Report the malaria status.
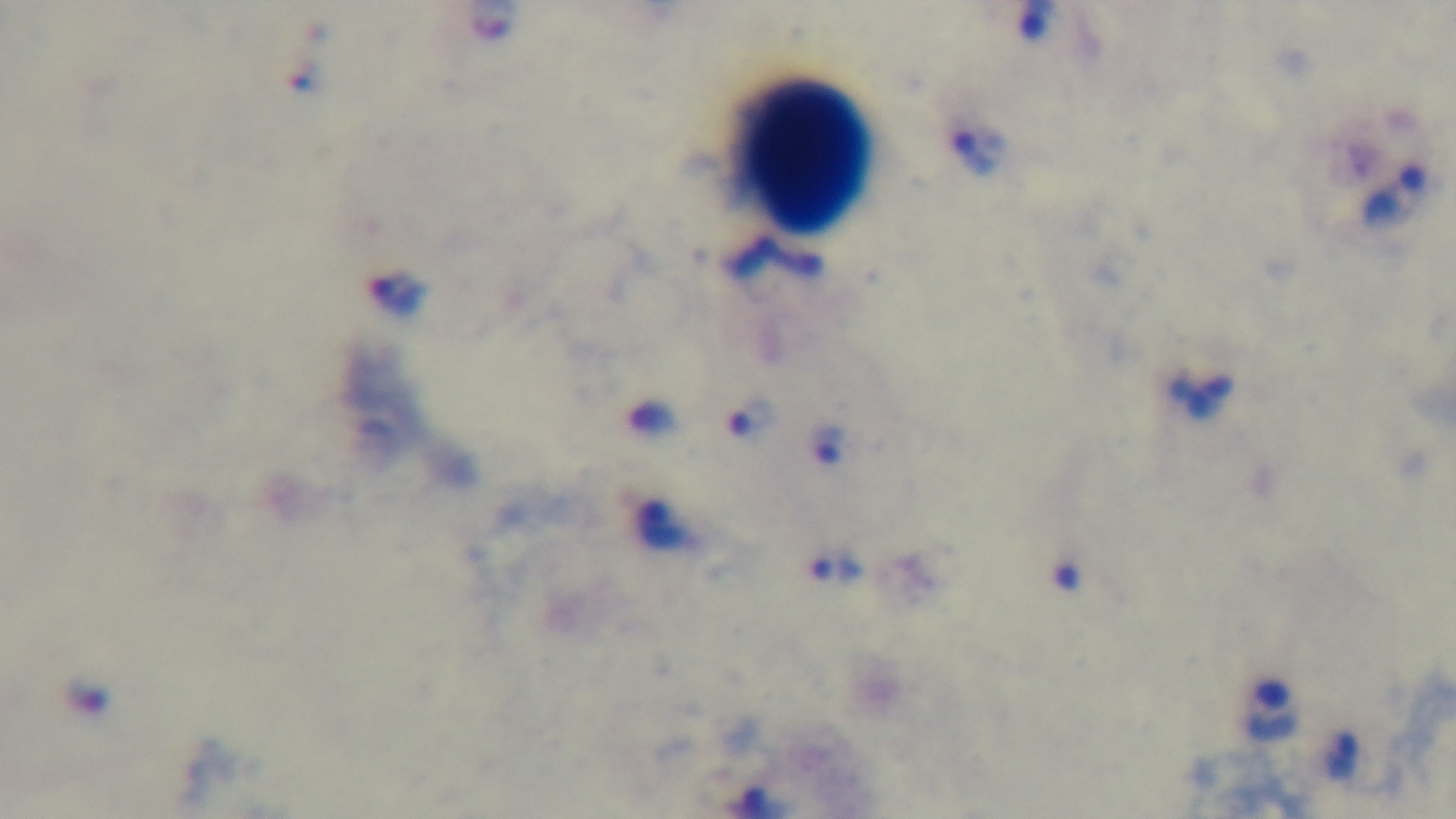

It is infected.

Summary:
  - Preparation: thick
  - Capture: mounted 4K digital camera
  - Field of view: single
  - Objective: 100x oil immersion
  - Modality: light microscopy
  - Stain: Giemsa